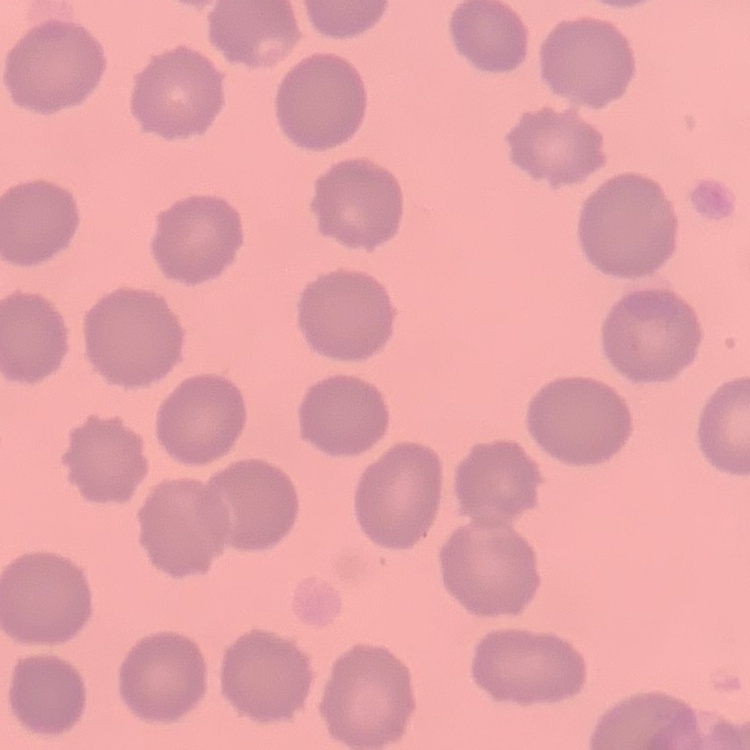
The red blood cells exhibit no rouleaux formation. Field's or Giemsa stain. One tile cut from a larger photomicrograph. Thin blood smear.